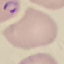 Malaria status: parasitized. Photographed with a smartphone camera at the microscope eyepiece. Giemsa stain. Thin blood smear. Cell patch, automatically extracted from a larger field of view and resized to 64 × 64 pixels.